Name the parasite shown.
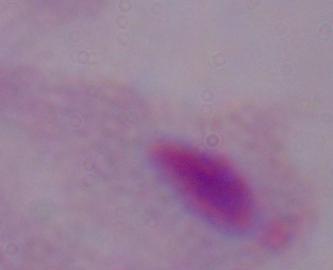

This is a trichomonad.

Micrograph. Captured at 1000x magnification.